Name the blood parasite species.
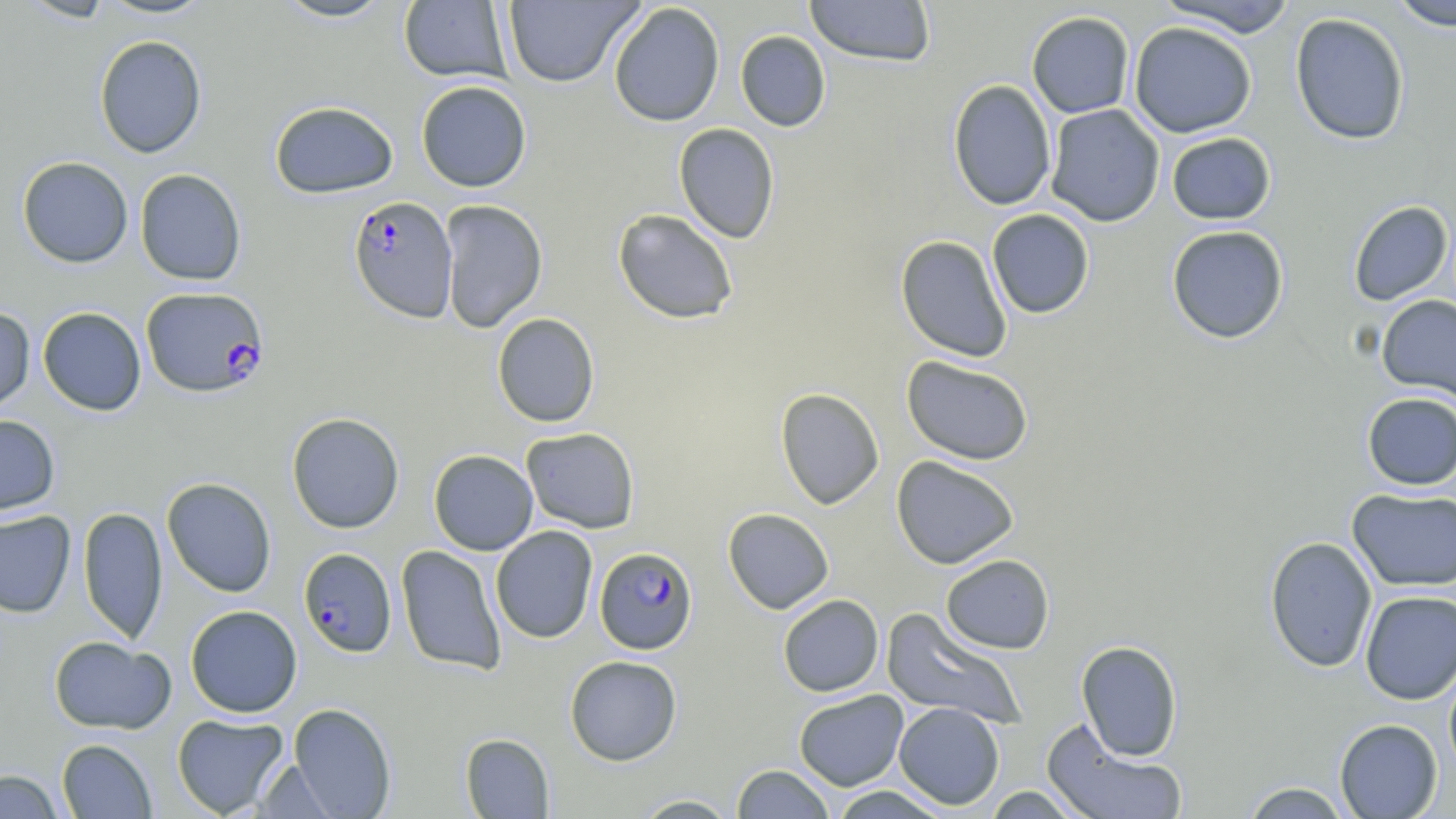

Plasmodium falciparum.

field of view = one of a larger specimen
modality = optical microscopy
image size = 1456×819 pixels
magnification = 1000x
preparation = thin blood film
Plasmodium falciparum-infected red blood cell locations = approximate bounding boxes as named x1/y1/x2/y2 corners in pixels: (x1=348, y1=194, x2=458, y2=323), (x1=140, y1=286, x2=268, y2=398), (x1=594, y1=547, x2=698, y2=654), (x1=298, y1=548, x2=397, y2=658)
stain = May-Grünwald-Giemsa
uninfected red blood cell locations = approximate bounding boxes as named x1/y1/x2/y2 corners in pixels: (x1=18, y1=0, x2=117, y2=22), (x1=95, y1=0, x2=215, y2=20), (x1=272, y1=0, x2=396, y2=23), (x1=503, y1=0, x2=644, y2=87), (x1=804, y1=0, x2=936, y2=67), (x1=399, y1=1, x2=512, y2=84), (x1=1154, y1=1, x2=1299, y2=37), (x1=1387, y1=1, x2=1456, y2=31), (x1=608, y1=2, x2=725, y2=127), (x1=1026, y1=11, x2=1135, y2=118), (x1=1289, y1=12, x2=1411, y2=145), (x1=1129, y1=21, x2=1257, y2=138), (x1=735, y1=31, x2=831, y2=132), (x1=93, y1=35, x2=207, y2=158), (x1=948, y1=79, x2=1057, y2=211), (x1=415, y1=80, x2=532, y2=192), (x1=269, y1=100, x2=399, y2=199), (x1=1046, y1=104, x2=1165, y2=227), (x1=674, y1=123, x2=780, y2=243), (x1=1166, y1=132, x2=1276, y2=225), (x1=17, y1=156, x2=133, y2=268), (x1=134, y1=168, x2=247, y2=286), (x1=438, y1=199, x2=548, y2=333), (x1=1348, y1=201, x2=1453, y2=306), (x1=612, y1=208, x2=739, y2=324), (x1=986, y1=209, x2=1095, y2=319), (x1=1166, y1=225, x2=1290, y2=344), (x1=895, y1=235, x2=1013, y2=362), (x1=1376, y1=294, x2=1456, y2=405), (x1=0, y1=305, x2=35, y2=415), (x1=38, y1=307, x2=146, y2=415), (x1=492, y1=312, x2=600, y2=427), (x1=901, y1=355, x2=1034, y2=466), (x1=775, y1=388, x2=884, y2=509), (x1=1361, y1=392, x2=1456, y2=490), (x1=286, y1=412, x2=405, y2=533), (x1=0, y1=414, x2=60, y2=517), (x1=521, y1=427, x2=640, y2=533), (x1=428, y1=449, x2=538, y2=555), (x1=891, y1=455, x2=1019, y2=569), (x1=161, y1=477, x2=277, y2=597), (x1=1347, y1=487, x2=1456, y2=592), (x1=78, y1=506, x2=168, y2=646), (x1=722, y1=508, x2=834, y2=614), (x1=0, y1=510, x2=76, y2=618), (x1=491, y1=526, x2=598, y2=643), (x1=1264, y1=536, x2=1378, y2=673), (x1=396, y1=545, x2=507, y2=675), (x1=941, y1=554, x2=1055, y2=654), (x1=1360, y1=590, x2=1456, y2=704), (x1=778, y1=594, x2=884, y2=697), (x1=185, y1=605, x2=302, y2=718), (x1=881, y1=607, x2=1028, y2=730), (x1=48, y1=635, x2=176, y2=734), (x1=1075, y1=640, x2=1183, y2=760), (x1=564, y1=655, x2=682, y2=765), (x1=1443, y1=658, x2=1456, y2=780), (x1=793, y1=690, x2=909, y2=791), (x1=894, y1=702, x2=1005, y2=810), (x1=288, y1=703, x2=397, y2=818), (x1=171, y1=713, x2=290, y2=817), (x1=1334, y1=718, x2=1443, y2=818), (x1=1041, y1=720, x2=1189, y2=819), (x1=460, y1=733, x2=554, y2=818), (x1=57, y1=738, x2=157, y2=818), (x1=254, y1=758, x2=340, y2=818), (x1=731, y1=765, x2=835, y2=818), (x1=1, y1=769, x2=66, y2=819), (x1=1239, y1=781, x2=1353, y2=818), (x1=828, y1=786, x2=951, y2=818), (x1=981, y1=786, x2=1088, y2=818), (x1=629, y1=794, x2=741, y2=818)